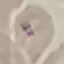

Malaria status: uninfected. Giemsa-stained preparation. Acquired by smartphone through the microscope eyepiece. Automatically extracted cell patch, resized to 64 × 64 pixels. Thin blood smear.